Identify the cell.
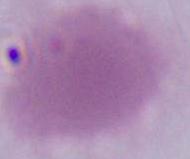
This is an erythrocyte.

Micrograph. 1000x magnification.